Point out malaria parasites and leukocytes.
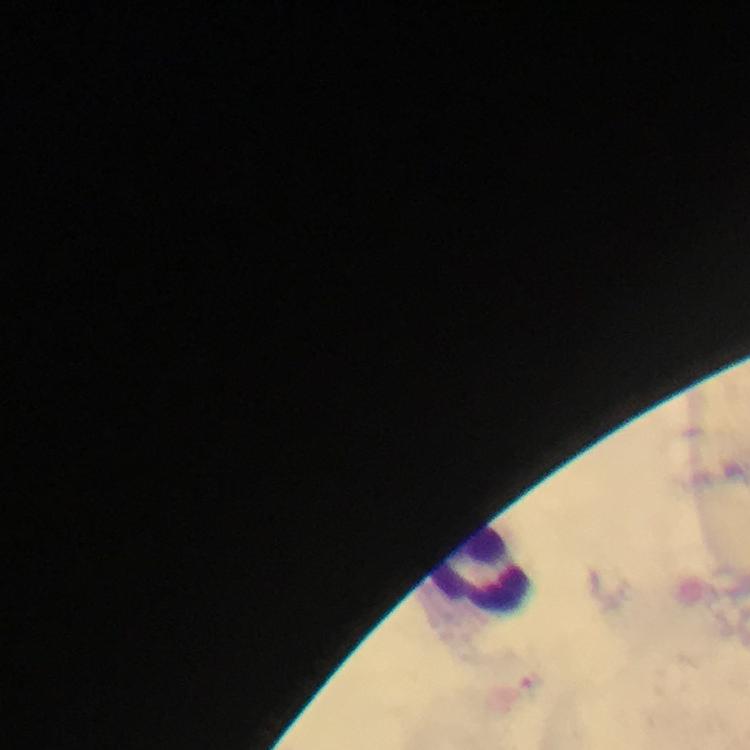
No malaria parasites detected.
Approximate centers as (x, y) in pixels.
Leukocytes: (481, 568).

Summary:
  - Cropped from: one field of view
  - Immersion oil: used
  - Capture: smartphone camera through the microscope
  - Context: from a diagnostic examination for malaria
  - Stain: Giemsa
  - Image size: 750×750 pixels
  - Preparation: thick smear
  - Magnification: 100x